State which parasite is depicted.
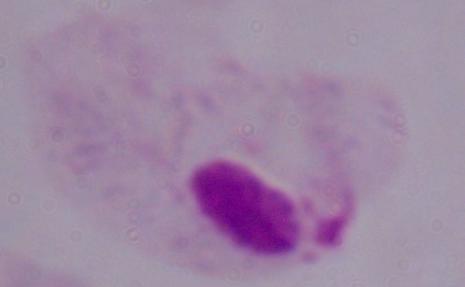
A trichomonad.

{
  "magnification": "1000x",
  "modality": "photomicrograph"
}